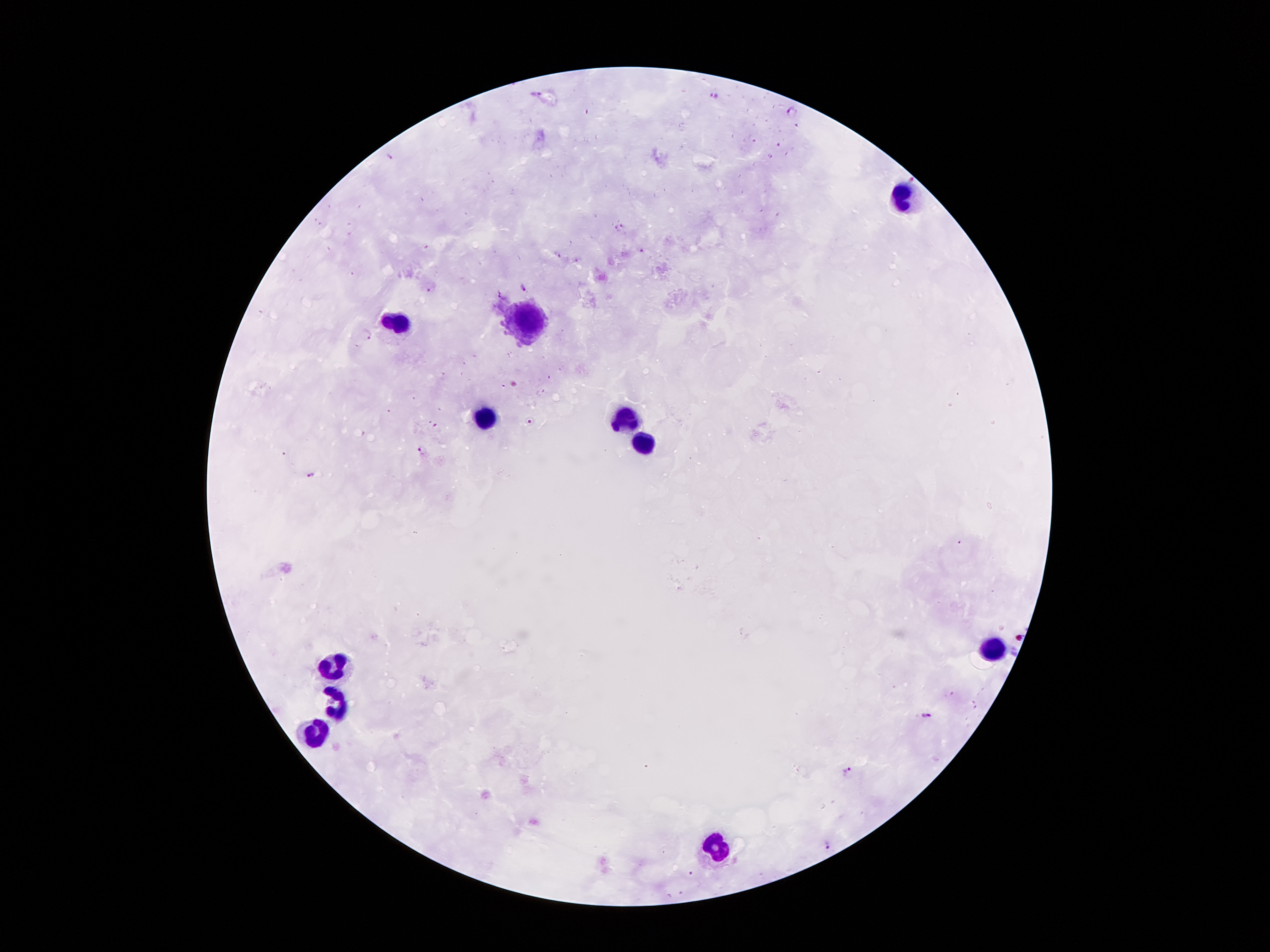
preparation: thick blood smear
field_of_view: single
capture: smartphone camera through the microscope eyepiece
stain: Giemsa
patient_malaria_status: infected with Plasmodium falciparum
image_size: 1270×952 pixels
magnification: 100x
leukocyte_locations: 'approximate object centers, in pixels from the top-left corner: (x=900, y=194), (x=524, y=318), (x=396, y=327), (x=483, y=418), (x=626, y=420), (x=639, y=436), (x=987, y=645), (x=334, y=666), (x=334, y=709), (x=315, y=735), (x=714, y=849)'
malaria_parasite_locations: 'approximate object centers, in pixels from the top-left corner: (x=537, y=94), (x=714, y=96), (x=792, y=111), (x=798, y=125), (x=780, y=145), (x=390, y=157), (x=912, y=177), (x=623, y=224), (x=615, y=228), (x=642, y=249), (x=557, y=254), (x=524, y=289), (x=428, y=291), (x=500, y=294), (x=368, y=334), (x=549, y=376), (x=504, y=385), (x=541, y=392), (x=530, y=422), (x=436, y=425), (x=422, y=449), (x=312, y=475), (x=926, y=715), (x=847, y=772), (x=828, y=843), (x=691, y=874)'